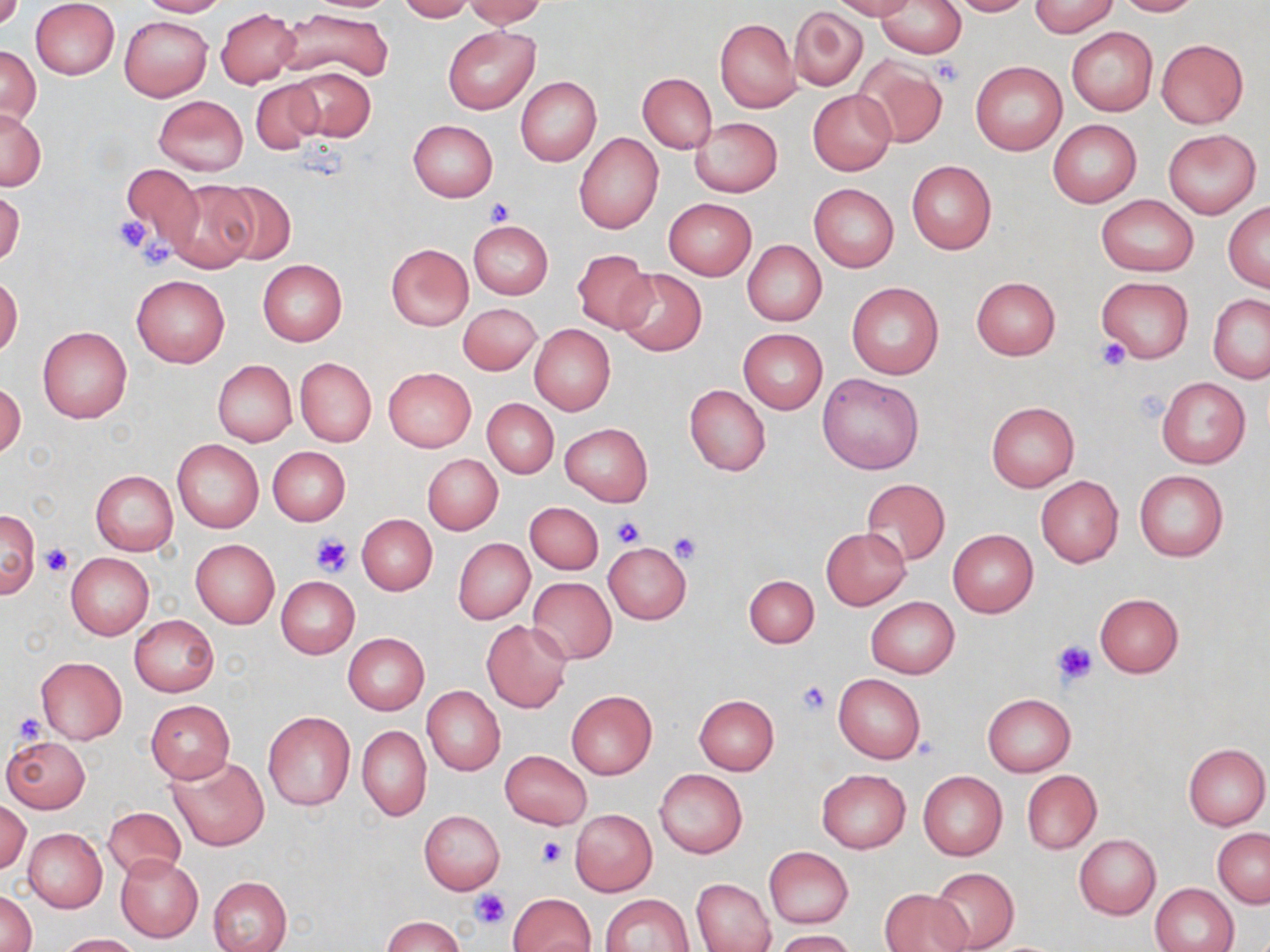

slide-level diagnosis = negative for blood parasites
uninfected red blood cell locations = approximate bounding boxes as (x1,y1)-(x2,y2) corner pairs in pixels: (136,0)-(229,17), (397,0)-(474,22), (463,0)-(548,27), (832,0)-(916,21), (876,0)-(966,58), (946,0)-(1033,16), (1030,0)-(1118,36), (1111,0)-(1201,16), (31,1)-(120,80), (790,7)-(867,91), (216,8)-(299,88), (277,8)-(393,84), (119,15)-(211,101), (715,18)-(800,114), (443,24)-(540,115), (1067,26)-(1157,116), (1156,39)-(1247,128), (0,45)-(41,129), (851,55)-(948,148), (971,60)-(1067,155), (286,66)-(376,143), (638,73)-(716,154), (516,77)-(601,167), (249,79)-(326,154), (808,89)-(897,175), (153,94)-(248,177), (0,107)-(44,190), (690,118)-(781,197), (1048,119)-(1141,208), (408,120)-(498,201), (1162,129)-(1261,219), (575,133)-(664,234), (907,160)-(996,254), (120,163)-(205,251), (162,178)-(258,273), (206,179)-(296,264), (809,184)-(898,271), (1,189)-(24,268), (1096,195)-(1199,277), (663,198)-(757,280), (1224,202)-(1270,291), (469,220)-(553,299), (742,240)-(827,326), (385,243)-(473,329), (573,249)-(654,333), (258,259)-(347,346), (615,268)-(707,356), (0,273)-(23,359), (131,275)-(229,367), (972,277)-(1061,359), (1097,277)-(1193,362), (846,282)-(943,379), (1208,294)-(1270,383), (458,303)-(542,375), (530,324)-(616,415), (37,326)-(132,424), (738,328)-(827,413), (295,357)-(376,447), (212,360)-(297,446), (384,367)-(476,452), (817,372)-(924,475), (1157,377)-(1250,469), (0,382)-(25,459), (686,384)-(771,477), (482,399)-(557,477), (986,401)-(1079,491), (560,422)-(652,506), (172,439)-(264,534), (268,446)-(351,526), (423,453)-(503,535), (1133,468)-(1229,562), (91,470)-(178,555), (1036,476)-(1123,567), (861,478)-(950,565), (525,502)-(604,574), (1,509)-(39,598), (357,514)-(438,595), (821,527)-(911,609), (947,529)-(1038,617), (453,538)-(535,624), (190,539)-(280,628), (602,542)-(692,623), (65,553)-(154,640), (743,574)-(819,647), (276,577)-(359,658), (528,578)-(616,664), (1094,593)-(1184,677), (866,597)-(960,679), (129,615)-(219,697), (482,619)-(572,712), (343,632)-(429,714), (36,657)-(127,743), (832,673)-(926,764), (422,686)-(505,775), (567,690)-(657,778), (982,693)-(1076,775), (694,694)-(779,774), (146,700)-(235,782), (263,711)-(356,811), (357,725)-(430,820), (2,735)-(91,813), (1183,744)-(1268,830), (500,750)-(592,829), (167,756)-(270,851), (655,769)-(747,858), (815,769)-(911,854), (1022,770)-(1101,854), (918,771)-(1006,860), (0,799)-(31,874), (103,805)-(186,880), (419,810)-(504,894), (571,810)-(657,896), (23,828)-(107,912), (1213,828)-(1269,907), (1074,834)-(1160,919), (764,847)-(853,928), (115,854)-(203,942), (928,867)-(1018,951), (207,876)-(292,952), (692,879)-(773,951), (1151,884)-(1238,952), (880,888)-(973,952), (1,890)-(35,952), (509,892)-(595,952), (603,893)-(693,951), (382,916)-(465,952), (773,930)-(857,952), (57,933)-(140,952)
preparation = thin blood film
modality = optical microscopy
image size = 1270×952 pixels
stain = May-Grünwald-Giemsa
magnification = 1000x
platelet locations = approximate bounding boxes as (x1,y1)-(x2,y2) corner pairs in pixels: (934,60)-(965,86), (485,197)-(515,224), (113,216)-(151,255), (144,239)-(179,269), (1095,338)-(1133,371), (612,516)-(645,549), (309,531)-(354,576), (668,532)-(702,566), (42,544)-(74,576), (1053,639)-(1098,686), (796,680)-(830,714), (11,711)-(45,744), (536,837)-(568,869), (471,888)-(510,928)
field of view = one of a larger specimen